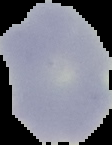

Summary:
  - Image size: 112×145 pixels
  - Image type: cell region segmented out of the field of view; surrounding area masked to black
  - Preparation: thin blood film
  - Result: no Plasmodium parasites detected